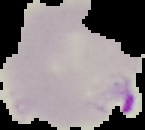

preparation = thin blood smear
result = Plasmodium parasites identified
image type = cell region segmented out of the field of view; surrounding area masked to black
image size = 145×130 pixels